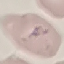

Summary:
  - Malaria status: parasitized
  - Stain: Giemsa
  - Preparation: thin smear
  - Capture: smartphone camera at the microscope eyepiece
  - Image type: automatically extracted cell patch, resized to 64 × 64 pixels